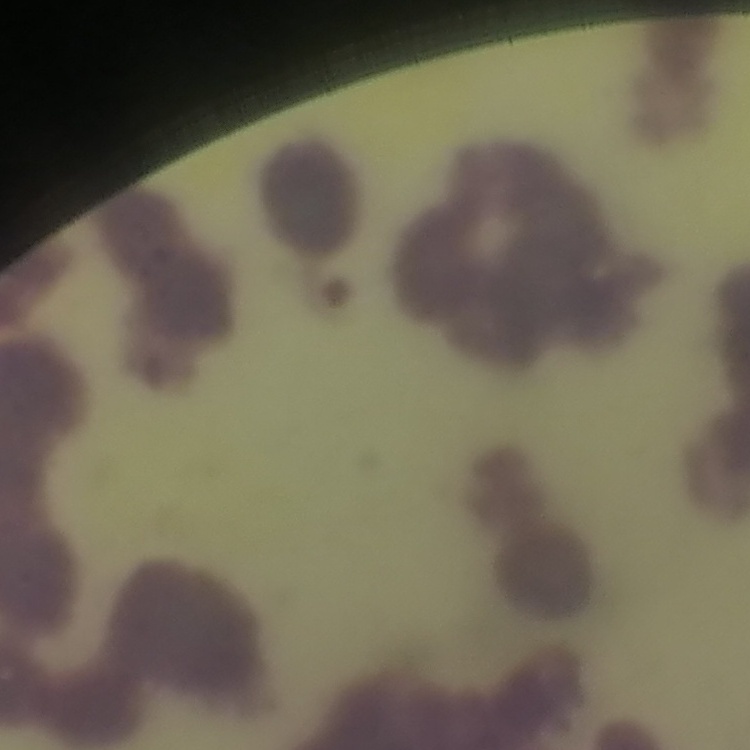
The red blood cells show rouleaux formation. Square crop of a larger photomicrograph. Field's or Giemsa stain. Thin peripheral smear.